Assess this cell for malaria.
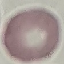

Uninfected.

image type = cell patch, automatically extracted from a larger field of view and resized to 64 × 64 pixels
stain = Giemsa
capture = smartphone through the microscope eyepiece
preparation = thin smear